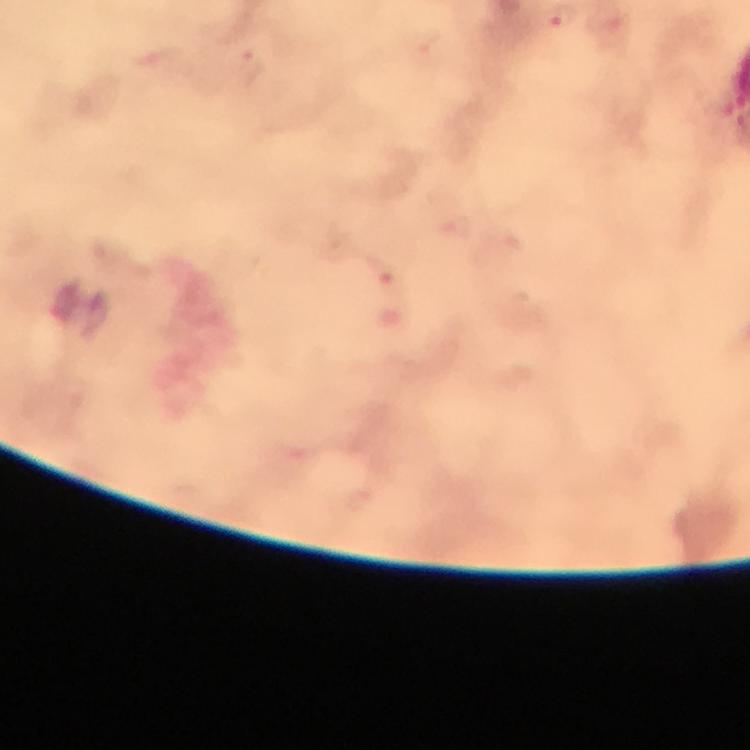

immersion oil = applied
malaria parasite locations = approximate centers as {x, y} in pixels: {250, 65}
stain = Giemsa
cropped from = a single field of view
capture = smartphone mounted on the microscope
context = from a diagnostic examination for malaria
image size = 750×750 pixels
magnification = 100x
preparation = thick blood smear